Assess this cell for malaria.
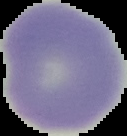
Uninfected.

preparation = thin blood smear
image type = segmented cell region with the area outside set to black
image size = 127×136 pixels